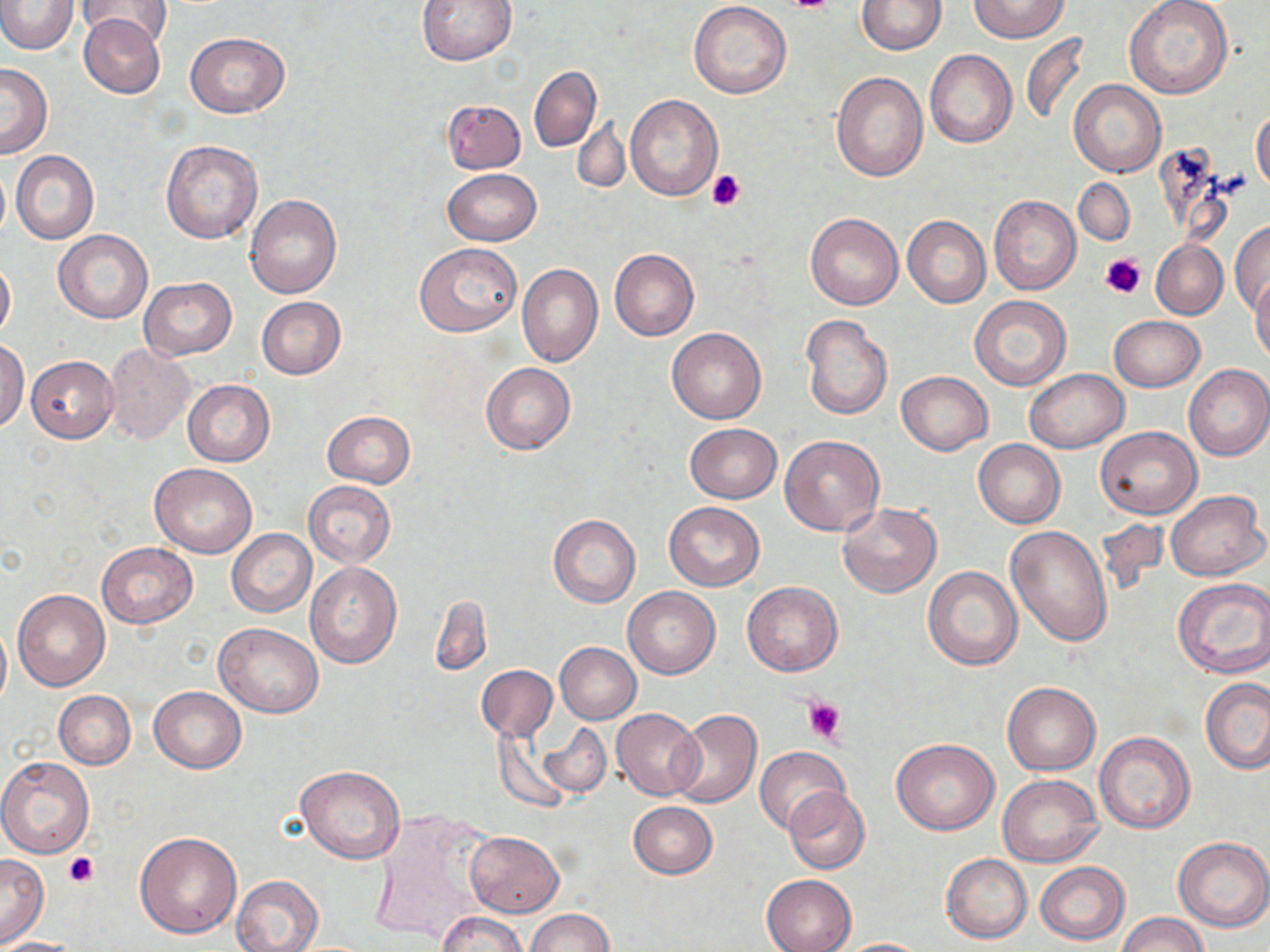
Approximate bounding boxes as (x1,y1)-(x2,y2) corner pairs in pixels. Uninfected red blood cell locations: (416,0)-(517,66), (969,0)-(1069,41), (1,1)-(77,53), (76,1)-(172,47), (857,1)-(946,54), (688,2)-(792,99), (1124,2)-(1232,100), (79,13)-(166,98), (185,32)-(290,117), (1020,33)-(1089,126), (925,50)-(1016,148), (0,63)-(52,158), (529,66)-(601,152), (831,71)-(928,182), (1069,80)-(1166,179), (625,96)-(721,199), (442,99)-(526,174), (1251,106)-(1270,195), (573,117)-(628,194), (162,140)-(263,245), (1153,146)-(1233,247), (12,151)-(99,244), (0,164)-(10,241), (444,168)-(541,245), (1074,177)-(1134,245), (245,195)-(341,298), (989,195)-(1081,295), (806,212)-(903,310), (902,215)-(991,307), (1231,221)-(1270,316), (53,229)-(153,323), (1151,241)-(1228,320), (416,244)-(521,337), (609,249)-(699,341), (0,256)-(15,344), (517,263)-(603,367), (140,277)-(237,360), (1252,277)-(1270,364), (970,295)-(1071,391), (256,297)-(346,379), (800,314)-(893,421), (1108,315)-(1205,392), (667,328)-(766,424), (0,340)-(28,431), (104,344)-(194,445), (25,356)-(119,442), (481,362)-(575,454), (1183,364)-(1270,461), (1024,369)-(1128,452), (895,371)-(991,455), (182,379)-(275,466), (322,410)-(415,487), (684,424)-(781,503), (1096,426)-(1202,518), (779,434)-(885,536), (974,439)-(1065,528), (150,463)-(257,558), (304,481)-(395,567), (1165,489)-(1267,581), (664,501)-(765,590), (837,502)-(941,598), (547,513)-(641,607), (1093,518)-(1168,598), (1006,525)-(1112,646), (227,529)-(315,616), (96,542)-(197,627), (305,562)-(402,668), (923,565)-(1023,669), (1173,577)-(1270,678), (742,582)-(842,676), (622,586)-(720,678), (12,588)-(110,690), (430,595)-(492,676), (0,619)-(11,714), (214,622)-(324,718), (554,642)-(641,724), (476,664)-(558,741), (1200,677)-(1270,774), (1002,681)-(1100,775), (148,687)-(246,773), (52,690)-(136,770), (611,708)-(703,800), (669,709)-(762,809), (539,723)-(611,799), (493,728)-(575,814), (1095,731)-(1196,834), (891,738)-(999,835), (755,746)-(850,836), (0,756)-(94,858), (296,765)-(406,863), (997,774)-(1102,868), (783,786)-(870,875), (627,801)-(717,878), (370,808)-(500,946), (466,830)-(563,917), (133,832)-(242,938), (1173,837)-(1270,932), (942,853)-(1032,943), (0,855)-(49,944), (1035,861)-(1130,945), (761,873)-(856,952), (232,875)-(324,952), (525,908)-(614,952), (436,912)-(527,952), (1117,913)-(1207,952), (0,937)-(81,951), (833,937)-(933,951). Platelet locations: (779,0)-(838,14), (706,169)-(747,213), (1099,253)-(1146,300), (803,696)-(846,746), (64,851)-(98,887). Slide-level diagnosis: negative for blood parasites. One field of a larger specimen. May-Grünwald-Giemsa-stained preparation. Image is 1270×952 pixels. 1000x magnification. Optical microscopy. Thin blood film.